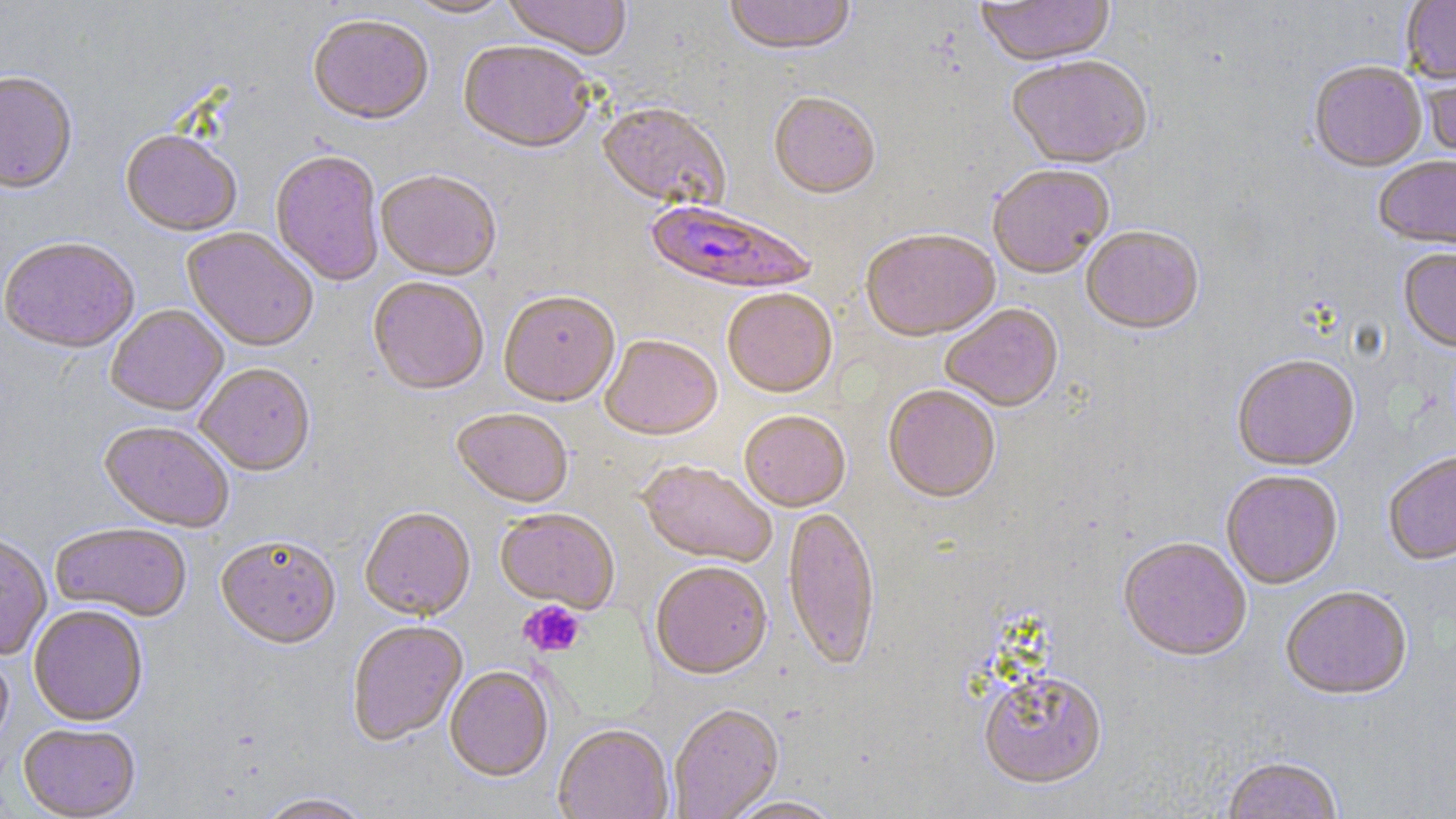
Approximate bounding boxes as [x1, y1, x2, y2] in pixels. Uninfected red blood cell locations: [403, 0, 515, 20], [502, 0, 632, 62], [723, 0, 856, 59], [976, 0, 1114, 70], [1401, 0, 1456, 86], [308, 17, 434, 129], [458, 44, 595, 157], [1006, 58, 1153, 172], [1309, 62, 1427, 175], [1420, 64, 1456, 166], [0, 74, 78, 197], [769, 95, 881, 202], [597, 104, 731, 213], [120, 133, 241, 239], [270, 152, 384, 287], [1374, 158, 1456, 253], [988, 167, 1114, 281], [375, 172, 501, 283], [1081, 228, 1204, 338], [181, 229, 319, 353], [861, 232, 1000, 344], [0, 240, 140, 355], [1398, 250, 1456, 356], [368, 279, 489, 397], [722, 291, 837, 401], [498, 293, 619, 409], [940, 305, 1064, 414], [106, 306, 229, 418], [600, 337, 722, 443], [1232, 357, 1360, 473], [195, 365, 315, 478], [883, 387, 1001, 505], [451, 411, 573, 511], [739, 413, 850, 514], [98, 422, 234, 534], [1383, 454, 1456, 568], [638, 461, 777, 568], [1221, 472, 1343, 591], [783, 507, 880, 675], [359, 509, 476, 623], [494, 510, 620, 612], [50, 525, 192, 623], [0, 533, 51, 661], [216, 538, 341, 652], [1118, 539, 1251, 665], [650, 563, 772, 682], [1281, 589, 1412, 702], [28, 606, 148, 727], [348, 623, 468, 748], [0, 650, 13, 755], [444, 667, 554, 784], [978, 673, 1109, 794], [668, 706, 784, 819], [18, 725, 141, 819], [553, 726, 674, 819], [1221, 759, 1344, 819], [256, 794, 373, 819], [724, 797, 845, 818]. Plasmodium falciparum-infected red blood cell locations: [644, 201, 816, 298]. Platelet locations: [519, 600, 586, 658]. Slide-level diagnosis: Plasmodium falciparum. Light microscopy. May-Grünwald-Giemsa stain. Captured at 1000x magnification. One field of a larger specimen. Image is 1456×819 pixels. Thin blood smear.